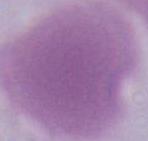 Captured at 1000x magnification. A red blood cell is seen. Micrograph.